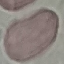
malaria_status: uninfected
stain: Giemsa
capture: smartphone through the microscope eyepiece
image_type: automatically extracted cell patch, resized to 64 × 64 pixels
preparation: thin blood smear